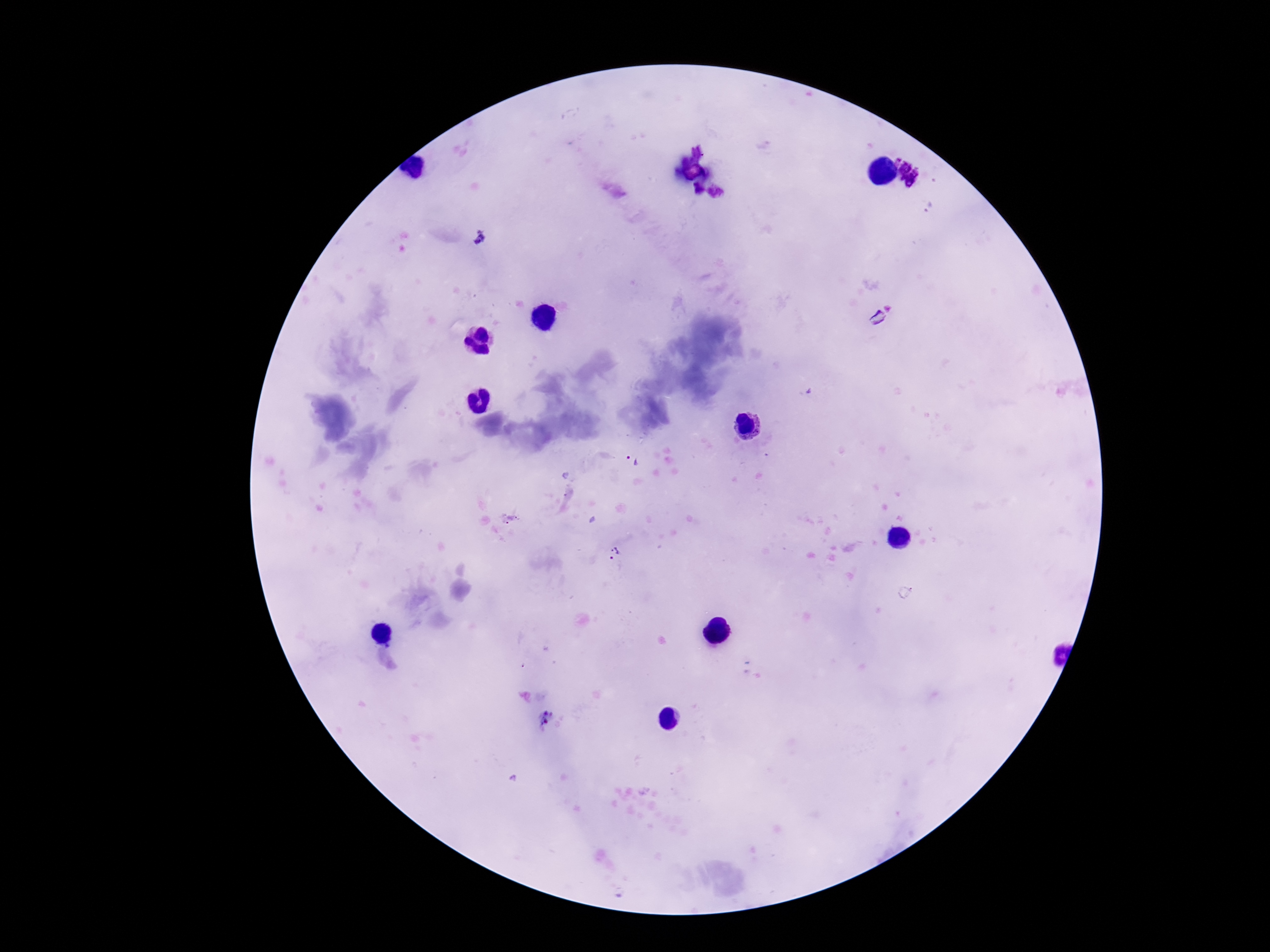

magnification = 100x
Plasmodium parasite locations = approximate centers as (x, y) in pixels: (698, 150), (906, 167), (695, 188), (716, 193), (480, 237), (878, 317), (632, 459), (614, 554), (546, 718)
patient malaria status = positive
field of view = single
preparation = thick blood film
stain = Giemsa
image size = 1270×952 pixels
capture = smartphone camera through the microscope eyepiece